Locate every white blood cell.
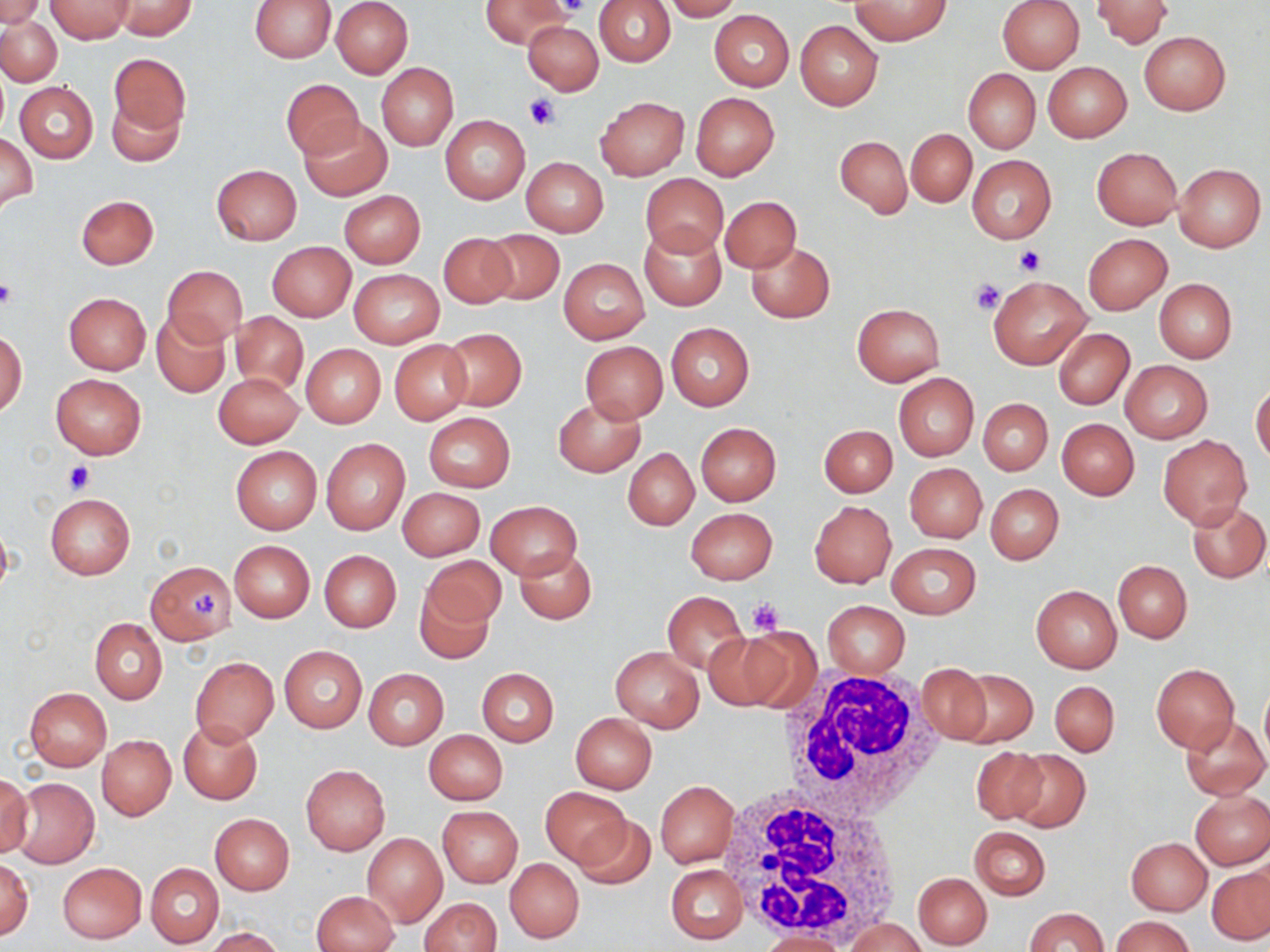

Approximate bounding boxes as (x1, y1, x2, y2) in pixels.
White blood cells: (778, 672, 942, 824), (719, 785, 905, 942).

{
  "slide_level_diagnosis": "no evidence of blood parasites",
  "modality": "optical microscopy",
  "platelet_locations": "approximate bounding boxes as (x1, y1, x2, y2) in pixels: (555, 0, 591, 17), (524, 93, 559, 131), (1012, 245, 1047, 275), (970, 278, 1004, 315), (0, 282, 17, 310), (62, 459, 98, 495), (189, 588, 222, 620), (746, 597, 782, 636)",
  "magnification": "1000x",
  "field_of_view": "single",
  "uninfected_red_blood_cell_locations": "approximate bounding boxes as (x1, y1, x2, y2) in pixels: (0, 0, 43, 29), (46, 0, 133, 42), (330, 0, 413, 79), (481, 0, 572, 50), (663, 0, 741, 21), (850, 0, 952, 45), (997, 0, 1084, 74), (1091, 0, 1172, 47), (110, 1, 197, 39), (249, 1, 335, 63), (592, 1, 675, 67), (709, 10, 793, 92), (1, 15, 62, 85), (522, 20, 604, 95), (795, 20, 883, 110), (1139, 31, 1231, 114), (107, 53, 189, 143), (1042, 61, 1132, 142), (376, 63, 458, 150), (964, 69, 1040, 153), (281, 78, 364, 159), (15, 81, 99, 163), (106, 90, 186, 168), (690, 92, 779, 181), (595, 96, 689, 181), (440, 115, 531, 205), (300, 116, 392, 200), (905, 128, 977, 208), (0, 133, 37, 208), (835, 135, 911, 218), (1092, 147, 1183, 229), (967, 154, 1057, 245), (521, 157, 608, 235), (1174, 163, 1266, 251), (212, 164, 301, 245), (640, 173, 729, 257), (340, 189, 425, 268), (75, 194, 159, 269), (720, 195, 801, 273), (639, 224, 727, 311), (483, 229, 565, 306), (438, 233, 517, 310), (1083, 233, 1172, 314), (746, 240, 835, 323), (268, 243, 356, 320), (559, 259, 648, 343), (163, 265, 247, 347), (349, 268, 444, 349), (989, 274, 1092, 370), (1154, 279, 1237, 362), (64, 292, 151, 374), (851, 303, 944, 385), (152, 310, 229, 397), (229, 310, 308, 395), (666, 322, 755, 410), (440, 327, 526, 411), (1053, 328, 1134, 409), (0, 329, 27, 418), (389, 340, 471, 422), (580, 341, 667, 423), (302, 345, 386, 427), (1119, 360, 1213, 443), (214, 372, 304, 448), (50, 373, 146, 460), (893, 373, 979, 460), (1251, 384, 1270, 464), (554, 397, 645, 476), (978, 398, 1052, 474), (424, 412, 516, 491), (1058, 418, 1139, 500), (695, 422, 781, 505), (819, 424, 897, 498), (1158, 435, 1252, 529), (321, 438, 410, 535), (230, 446, 322, 535), (624, 448, 699, 530), (905, 463, 987, 542), (986, 483, 1063, 565), (399, 488, 485, 560), (45, 493, 136, 579), (486, 500, 582, 579), (1187, 500, 1269, 582), (810, 501, 897, 588), (685, 507, 778, 584), (0, 518, 14, 603), (228, 540, 315, 622), (886, 542, 981, 618), (514, 546, 597, 624), (319, 550, 401, 632), (420, 554, 505, 633), (1113, 560, 1192, 642), (147, 562, 237, 645), (415, 584, 496, 664), (1030, 585, 1122, 673), (662, 592, 747, 673), (822, 601, 909, 677), (90, 617, 168, 705), (724, 626, 822, 713), (279, 646, 366, 732), (610, 646, 704, 732), (191, 657, 278, 745), (917, 664, 992, 742), (1151, 664, 1238, 754), (477, 667, 559, 746), (364, 668, 448, 749), (953, 670, 1037, 749), (1050, 681, 1120, 756), (1260, 684, 1270, 762), (25, 688, 111, 770), (570, 712, 657, 794), (1182, 715, 1269, 801), (178, 719, 263, 804), (424, 729, 508, 804), (97, 734, 176, 820), (971, 747, 1049, 825), (1005, 750, 1090, 833), (300, 764, 390, 854), (0, 771, 34, 858), (13, 777, 100, 868), (655, 780, 738, 867), (541, 786, 630, 868), (1191, 791, 1270, 869), (437, 806, 522, 887), (209, 813, 294, 895), (573, 814, 656, 892), (970, 826, 1050, 899), (362, 833, 446, 926), (1127, 838, 1211, 915), (1, 857, 34, 940), (505, 858, 584, 943), (57, 862, 146, 943), (146, 864, 224, 950), (666, 864, 748, 944), (1208, 865, 1270, 946), (913, 872, 992, 949), (311, 890, 398, 952), (420, 897, 501, 952), (1024, 906, 1109, 952), (1112, 915, 1194, 952), (847, 916, 927, 952), (207, 928, 286, 952), (759, 928, 844, 952)",
  "stain": "May-Grünwald-Giemsa",
  "image_size": "1270×952 pixels",
  "preparation": "thin blood smear"
}